Classify this cell by malaria status.
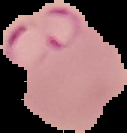
Parasitized.

image size = 127×133 pixels
image type = cell region segmented out of the field of view; surrounding area masked to black
preparation = thin blood film